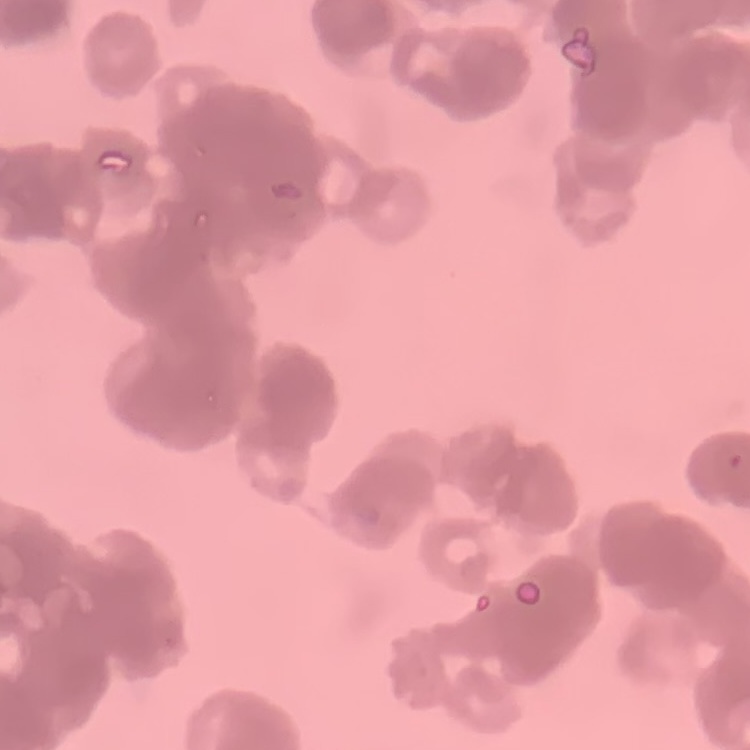
{
  "erythrocyte_morphology": "rouleaux formation",
  "stain": "Field's or Giemsa",
  "preparation": "thin blood smear",
  "image_type": "square crop of a larger photomicrograph"
}